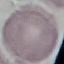

result = no malaria parasites detected
stain = Giemsa
capture = smartphone through the microscope eyepiece
preparation = thin blood smear
image type = automatically extracted cell patch, resized to 64 × 64 pixels